Identify the blood parasite species.
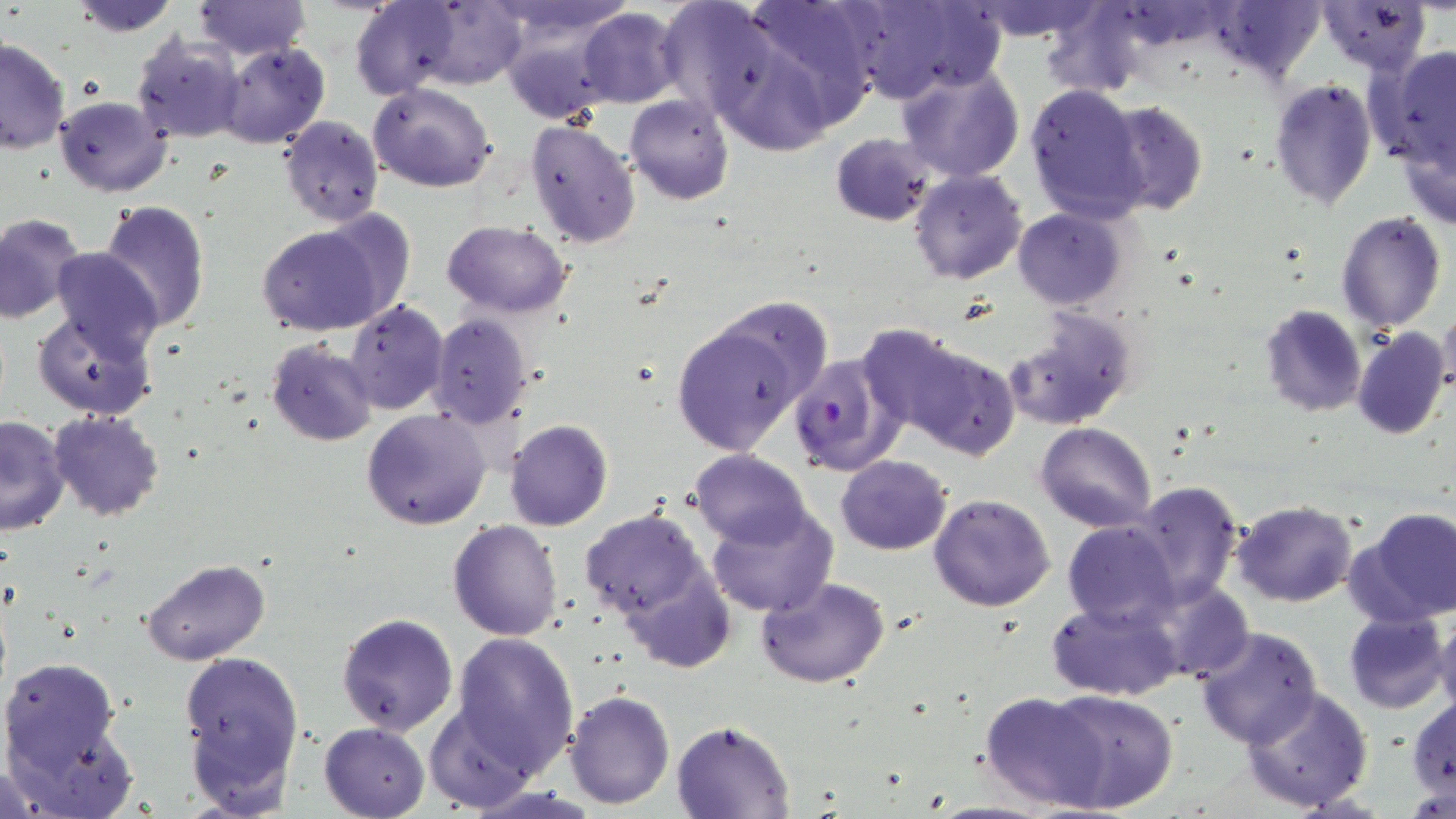

Plasmodium falciparum.

Approximate bounding boxes as (x1, y1, x2, y2) in pixels. Plasmodium falciparum-infected red blood cell locations: (788, 352, 904, 475). Uninfected red blood cell locations: (68, 0, 181, 37), (190, 0, 311, 60), (350, 0, 466, 100), (704, 0, 873, 147), (965, 0, 1106, 42), (842, 1, 995, 106), (1039, 2, 1156, 97), (1202, 2, 1327, 81), (1317, 2, 1430, 76), (576, 9, 683, 108), (499, 13, 620, 122), (130, 33, 244, 145), (0, 37, 70, 155), (215, 42, 329, 150), (1367, 47, 1456, 172), (895, 63, 1025, 184), (1269, 76, 1378, 212), (368, 83, 497, 192), (1023, 83, 1148, 220), (624, 95, 734, 205), (56, 97, 170, 197), (1103, 100, 1208, 218), (278, 115, 384, 227), (525, 117, 641, 250), (830, 132, 939, 227), (1398, 135, 1456, 231), (908, 169, 1028, 285), (99, 200, 211, 333), (1013, 206, 1129, 310), (1335, 211, 1447, 332), (0, 213, 86, 324), (256, 219, 399, 338), (442, 219, 574, 315), (52, 247, 164, 361), (344, 300, 448, 414), (1260, 304, 1366, 418), (1438, 305, 1456, 401), (1004, 307, 1139, 430), (33, 309, 158, 421), (670, 313, 818, 457), (428, 314, 535, 428), (854, 323, 986, 441), (1352, 327, 1449, 441), (892, 339, 1021, 460), (265, 340, 380, 448), (361, 408, 492, 530), (48, 413, 164, 521), (0, 415, 69, 534), (505, 420, 613, 531), (1036, 422, 1157, 532), (689, 450, 814, 548), (835, 456, 953, 555), (1129, 480, 1244, 604), (928, 492, 1056, 611), (1229, 499, 1359, 608), (706, 501, 840, 619), (578, 507, 713, 623), (1353, 509, 1456, 626), (448, 520, 563, 641), (1063, 522, 1182, 629), (143, 558, 270, 666), (621, 568, 734, 675), (756, 575, 891, 688), (1154, 580, 1252, 683), (1046, 598, 1184, 701), (1432, 609, 1456, 716), (1343, 611, 1448, 713), (335, 613, 458, 736), (1195, 627, 1323, 749), (449, 632, 580, 775), (180, 648, 303, 807), (1, 656, 135, 812), (1240, 686, 1375, 814), (1044, 688, 1178, 814), (566, 689, 675, 809), (979, 690, 1108, 812), (1408, 698, 1455, 797), (427, 705, 536, 811), (672, 719, 796, 817), (319, 722, 431, 818). One field of a larger specimen. May-Grünwald-Giemsa-stained preparation. Thin blood film. Image is 1456×819 pixels. Light microscopy. 1000x magnification.